State which parasite is depicted.
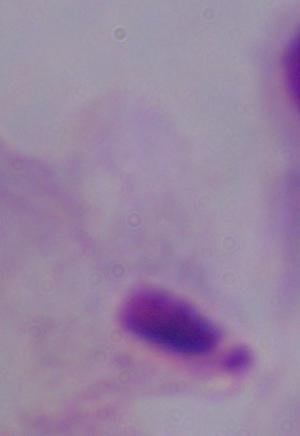
This is a trichomonad.

magnification: 1000x
modality: photomicrograph